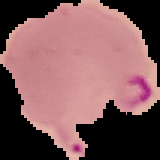

Cell region segmented out of the field of view; the surrounding area is masked to black. From a thin blood smear. Result: Plasmodium parasites detected. Image is 160×160 pixels.